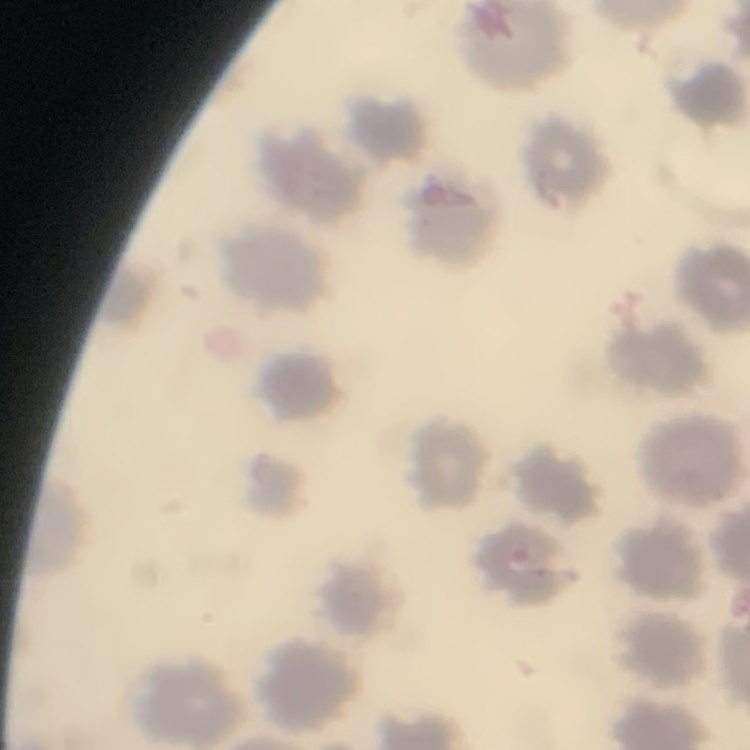

red_blood_cell_morphology: no rouleaux formation
image_type: one tile cut from a larger photomicrograph
stain: Field's or Giemsa
preparation: thin blood smear